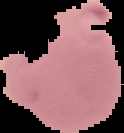
preparation = thin blood film
image size = 124×133 pixels
result = malaria parasites identified
image type = segmented cell region on a black background